Point out each malaria parasite and classify it by life-cycle stage.
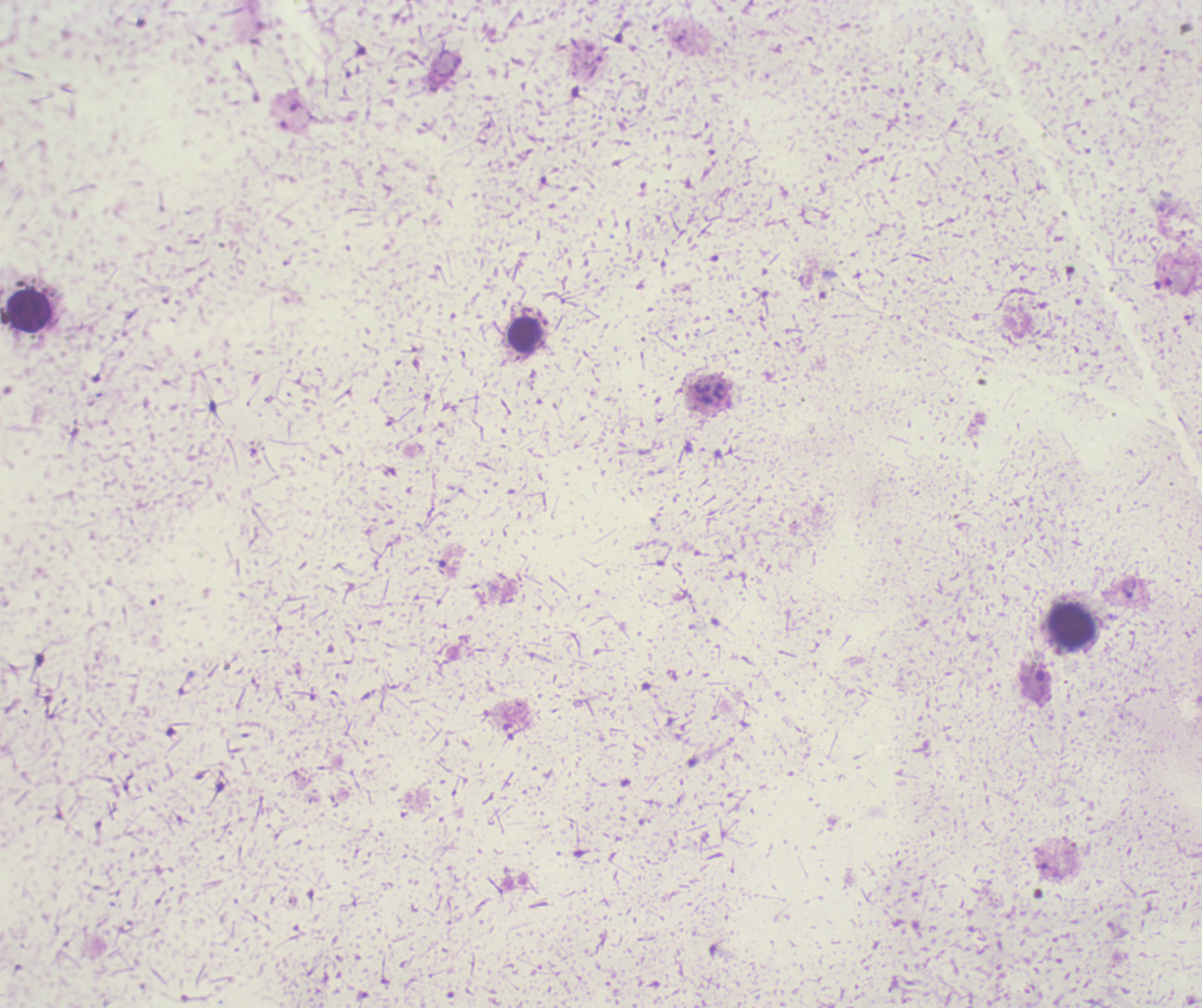
Approximate centers as (x, y) in pixels.
Trophozoites: (1128, 591).
No schizont or gametocyte forms observed.

Approximate centers as (x, y) in pixels. Leukocyte locations: (28, 310), (524, 335), (1072, 626). Previously used in an actual diagnosis. Romanowsky stain. Background quality: unsatisfactory. Thick blood smear. Captured at 100x magnification. Single field of view. Image is 1202×1008 pixels.